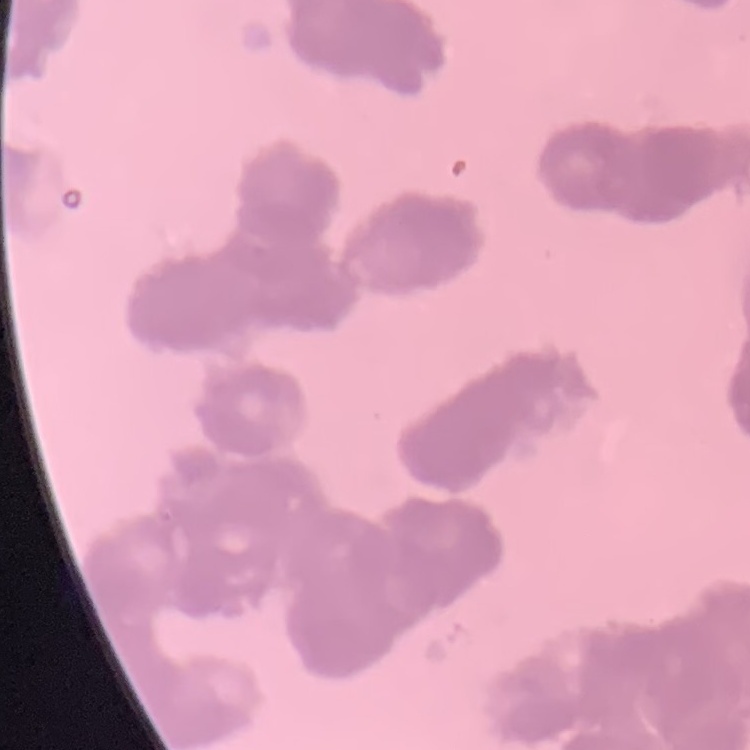

The erythrocytes show rouleaux formation. One tile cut from a larger photomicrograph. Thin blood smear. Stained with either Field's or Giemsa.